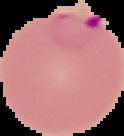

image type = segmented cell region on a black background
image size = 124×136 pixels
result = malaria parasites identified
preparation = thin blood film